Outline each blood parasite and name the species.
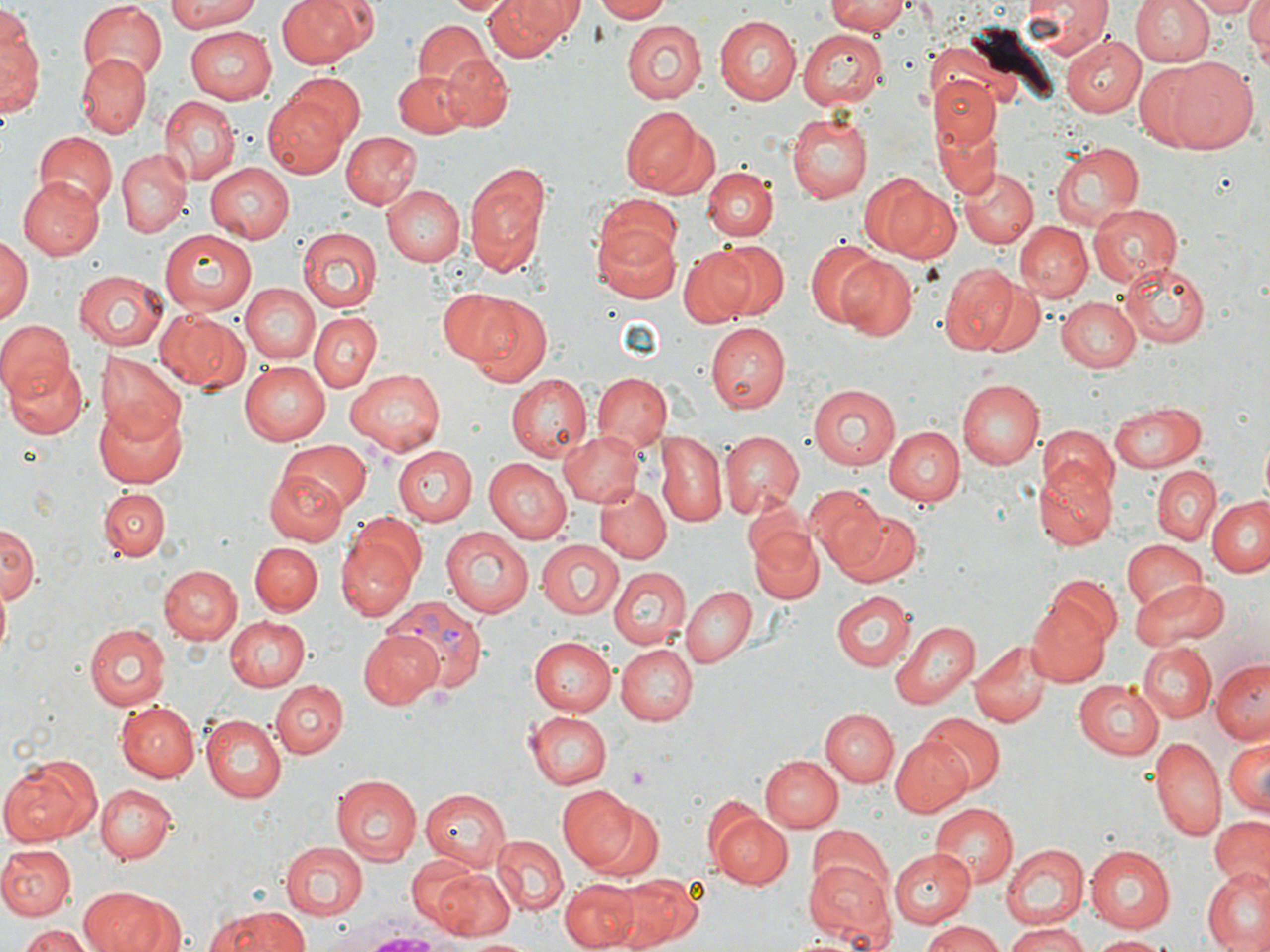

Approximate bounding boxes as named x1/y1/x2/y2 corners in pixels.
Plasmodium vivax-infected red blood cells: (x1=385, y1=596, x2=490, y2=695).
No Plasmodium falciparum, Plasmodium ovale, Plasmodium malariae, Babesia divergens, or Trypanosoma brucei observed.

{
  "slide_level_diagnosis": "Plasmodium vivax",
  "field_of_view": "single",
  "magnification": "1000x",
  "image_size": "1270×952 pixels",
  "preparation": "thin blood smear",
  "uninfected_red_blood_cell_locations": "approximate bounding boxes as named x1/y1/x2/y2 corners in pixels: (x1=164, y1=0, x2=270, y2=30), (x1=280, y1=0, x2=368, y2=67), (x1=445, y1=0, x2=516, y2=17), (x1=485, y1=0, x2=580, y2=62), (x1=592, y1=0, x2=671, y2=21), (x1=825, y1=0, x2=909, y2=36), (x1=1024, y1=0, x2=1109, y2=60), (x1=1129, y1=0, x2=1215, y2=66), (x1=1191, y1=0, x2=1259, y2=17), (x1=1245, y1=0, x2=1270, y2=55), (x1=76, y1=3, x2=166, y2=84), (x1=1, y1=4, x2=40, y2=115), (x1=713, y1=15, x2=801, y2=105), (x1=620, y1=19, x2=709, y2=102), (x1=412, y1=22, x2=493, y2=96), (x1=186, y1=25, x2=277, y2=104), (x1=799, y1=26, x2=889, y2=110), (x1=1059, y1=33, x2=1145, y2=117), (x1=75, y1=53, x2=152, y2=136), (x1=437, y1=53, x2=512, y2=131), (x1=1164, y1=56, x2=1259, y2=155), (x1=1132, y1=64, x2=1216, y2=150), (x1=392, y1=70, x2=472, y2=137), (x1=284, y1=72, x2=367, y2=149), (x1=933, y1=74, x2=997, y2=146), (x1=158, y1=94, x2=241, y2=183), (x1=265, y1=94, x2=349, y2=176), (x1=621, y1=106, x2=709, y2=197), (x1=786, y1=113, x2=873, y2=203), (x1=936, y1=121, x2=1002, y2=197), (x1=341, y1=131, x2=422, y2=208), (x1=32, y1=133, x2=116, y2=214), (x1=1050, y1=140, x2=1144, y2=230), (x1=117, y1=148, x2=191, y2=237), (x1=205, y1=161, x2=294, y2=244), (x1=461, y1=161, x2=552, y2=278), (x1=961, y1=166, x2=1037, y2=249), (x1=704, y1=167, x2=777, y2=239), (x1=865, y1=172, x2=956, y2=262), (x1=16, y1=180, x2=105, y2=260), (x1=381, y1=185, x2=465, y2=266), (x1=595, y1=196, x2=684, y2=271), (x1=1088, y1=202, x2=1184, y2=287), (x1=593, y1=221, x2=682, y2=303), (x1=1016, y1=221, x2=1093, y2=302), (x1=159, y1=230, x2=260, y2=317), (x1=296, y1=230, x2=381, y2=313), (x1=0, y1=234, x2=31, y2=331), (x1=804, y1=239, x2=887, y2=330), (x1=714, y1=240, x2=791, y2=321), (x1=678, y1=243, x2=761, y2=327), (x1=837, y1=255, x2=919, y2=341), (x1=1120, y1=260, x2=1210, y2=349), (x1=937, y1=261, x2=1021, y2=354), (x1=73, y1=270, x2=168, y2=350), (x1=973, y1=278, x2=1046, y2=357), (x1=240, y1=283, x2=318, y2=364), (x1=453, y1=292, x2=554, y2=386), (x1=1057, y1=297, x2=1142, y2=373), (x1=155, y1=307, x2=250, y2=393), (x1=310, y1=312, x2=381, y2=392), (x1=1, y1=319, x2=76, y2=404), (x1=707, y1=322, x2=789, y2=413), (x1=3, y1=344, x2=87, y2=438), (x1=96, y1=351, x2=188, y2=445), (x1=240, y1=361, x2=335, y2=446), (x1=346, y1=369, x2=445, y2=456), (x1=592, y1=373, x2=670, y2=454), (x1=506, y1=374, x2=592, y2=459), (x1=959, y1=377, x2=1043, y2=468), (x1=808, y1=383, x2=901, y2=470), (x1=1110, y1=400, x2=1206, y2=472), (x1=93, y1=402, x2=187, y2=489), (x1=1039, y1=422, x2=1117, y2=505), (x1=885, y1=426, x2=964, y2=507), (x1=559, y1=429, x2=645, y2=506), (x1=657, y1=429, x2=726, y2=527), (x1=717, y1=430, x2=806, y2=522), (x1=279, y1=438, x2=370, y2=514), (x1=392, y1=445, x2=478, y2=525), (x1=485, y1=458, x2=571, y2=543), (x1=1036, y1=461, x2=1116, y2=550), (x1=1152, y1=467, x2=1220, y2=545), (x1=264, y1=471, x2=349, y2=547), (x1=596, y1=485, x2=670, y2=563), (x1=807, y1=487, x2=890, y2=576), (x1=99, y1=489, x2=168, y2=561), (x1=1209, y1=496, x2=1270, y2=578), (x1=836, y1=508, x2=922, y2=588), (x1=349, y1=512, x2=426, y2=589), (x1=0, y1=523, x2=37, y2=607), (x1=747, y1=523, x2=823, y2=606), (x1=440, y1=525, x2=534, y2=616), (x1=335, y1=533, x2=417, y2=621), (x1=536, y1=539, x2=624, y2=618), (x1=1122, y1=540, x2=1209, y2=618), (x1=251, y1=543, x2=321, y2=615), (x1=157, y1=564, x2=242, y2=645), (x1=610, y1=566, x2=690, y2=649), (x1=1044, y1=572, x2=1123, y2=651), (x1=1130, y1=579, x2=1228, y2=648), (x1=681, y1=586, x2=756, y2=668), (x1=830, y1=592, x2=915, y2=672), (x1=1027, y1=596, x2=1113, y2=687), (x1=225, y1=617, x2=311, y2=691), (x1=891, y1=621, x2=977, y2=709), (x1=84, y1=622, x2=171, y2=712), (x1=357, y1=628, x2=442, y2=710), (x1=531, y1=636, x2=618, y2=715), (x1=969, y1=638, x2=1050, y2=728), (x1=615, y1=643, x2=697, y2=725), (x1=1140, y1=644, x2=1216, y2=722), (x1=1211, y1=659, x2=1270, y2=745), (x1=1074, y1=679, x2=1164, y2=759), (x1=271, y1=680, x2=348, y2=760), (x1=117, y1=700, x2=201, y2=782), (x1=821, y1=708, x2=899, y2=788), (x1=525, y1=712, x2=613, y2=788), (x1=920, y1=714, x2=1004, y2=794), (x1=200, y1=715, x2=287, y2=803), (x1=890, y1=736, x2=972, y2=818), (x1=1150, y1=736, x2=1223, y2=840), (x1=1223, y1=736, x2=1270, y2=816), (x1=1, y1=754, x2=101, y2=846), (x1=760, y1=754, x2=841, y2=833), (x1=329, y1=774, x2=422, y2=865), (x1=95, y1=783, x2=175, y2=862), (x1=555, y1=784, x2=644, y2=872), (x1=419, y1=786, x2=511, y2=868), (x1=586, y1=800, x2=665, y2=879), (x1=930, y1=805, x2=1016, y2=888), (x1=711, y1=810, x2=794, y2=890), (x1=1207, y1=814, x2=1270, y2=886), (x1=808, y1=823, x2=891, y2=900), (x1=491, y1=837, x2=568, y2=917), (x1=280, y1=842, x2=368, y2=918), (x1=1001, y1=842, x2=1088, y2=930), (x1=0, y1=845, x2=75, y2=919), (x1=1084, y1=845, x2=1176, y2=932), (x1=889, y1=850, x2=977, y2=927), (x1=404, y1=855, x2=483, y2=932), (x1=805, y1=858, x2=894, y2=943), (x1=430, y1=865, x2=517, y2=941), (x1=1202, y1=871, x2=1270, y2=951), (x1=611, y1=872, x2=702, y2=949), (x1=560, y1=877, x2=639, y2=951), (x1=82, y1=887, x2=179, y2=952), (x1=213, y1=907, x2=313, y2=951), (x1=918, y1=920, x2=1003, y2=952), (x1=1001, y1=922, x2=1092, y2=952), (x1=19, y1=924, x2=96, y2=952), (x1=1090, y1=933, x2=1170, y2=951), (x1=465, y1=937, x2=536, y2=952)",
  "modality": "light microscopy",
  "platelet_locations": "approximate bounding boxes as named x1/y1/x2/y2 corners in pixels: (x1=625, y1=766, x2=652, y2=789)",
  "stain": "May-Grünwald-Giemsa"
}